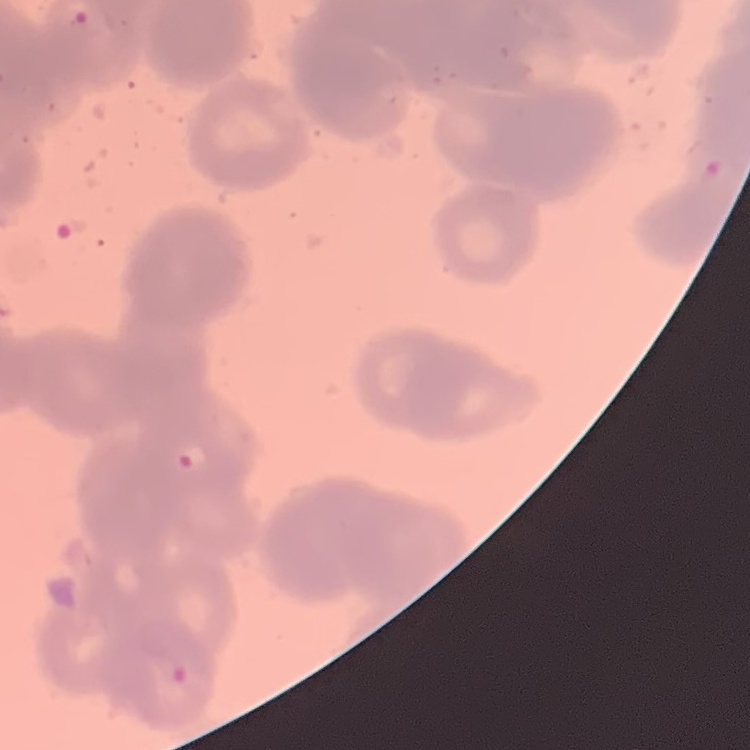 The erythrocytes exhibit rouleaux formation. Thin peripheral smear. Stained with either Field's or Giemsa. One tile cut from a larger photomicrograph.